Describe the morphology of the erythrocytes.
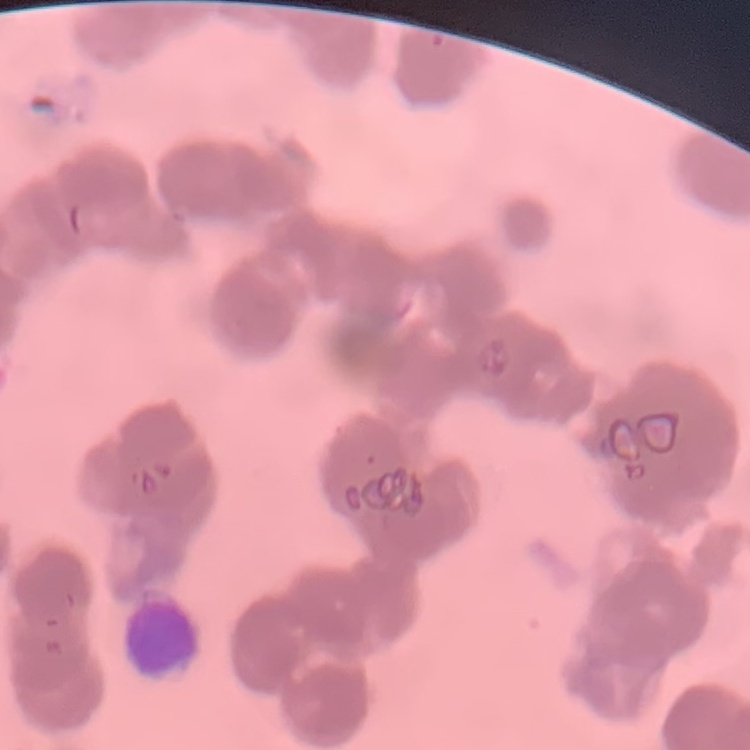
Rouleaux formation.

stain = Field's or Giemsa
preparation = thin blood film
image type = one tile cut from a larger photomicrograph